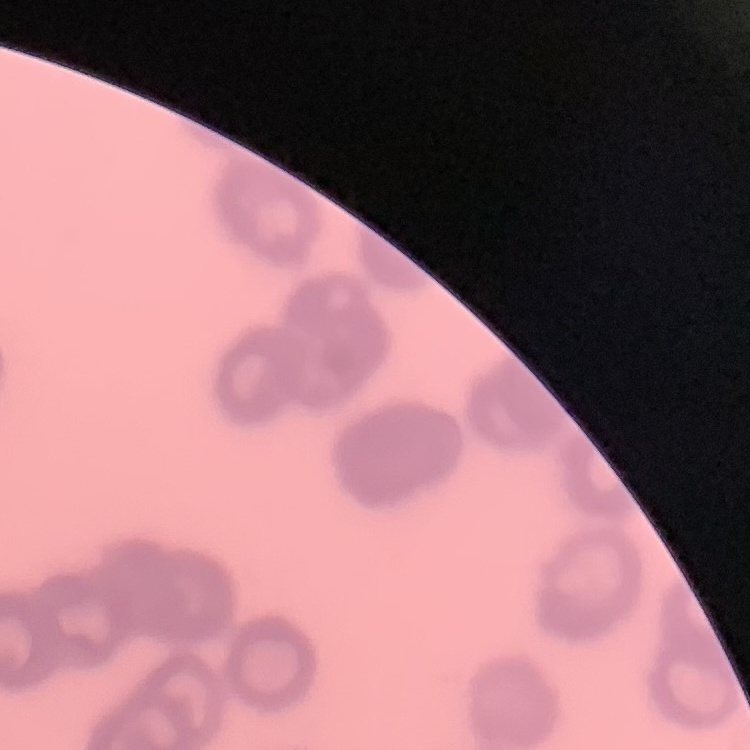
{
  "red_blood_cell_morphology": "rouleaux formation",
  "preparation": "thin blood smear",
  "image_type": "one tile cut from a larger photomicrograph",
  "stain": "Field's or Giemsa"
}